Assess this cell for malaria.
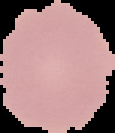

Uninfected.

Summary:
  - Preparation: thin blood film
  - Image size: 115×133 pixels
  - Image type: segmented cell region on a black background